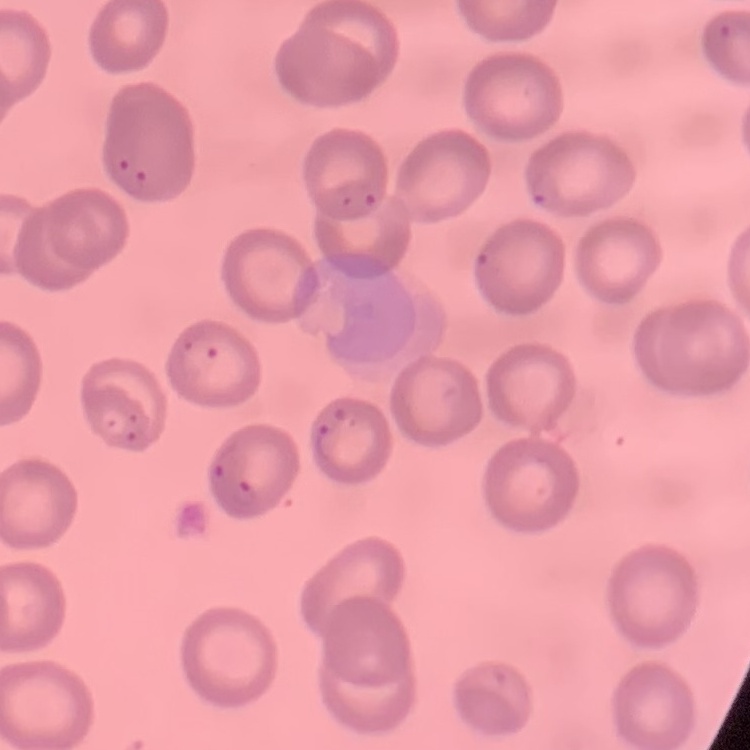
The red blood cells show no rouleaux formation. Field's or Giemsa stain. Thin blood film. One tile cut from a larger photomicrograph.